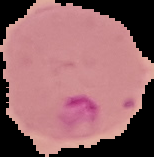
From a thin blood smear. Malaria status: parasitized. The area outside the segmented cell region is set to black. Image is 154×157 pixels.